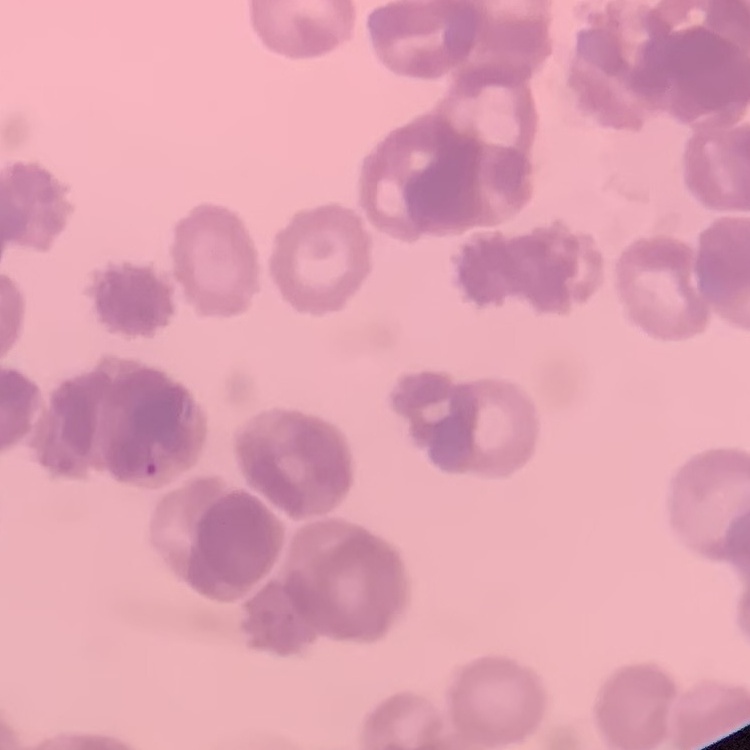
erythrocyte_morphology: rouleaux formation
stain: Field's or Giemsa
preparation: thin blood smear
image_type: square crop of a larger photomicrograph